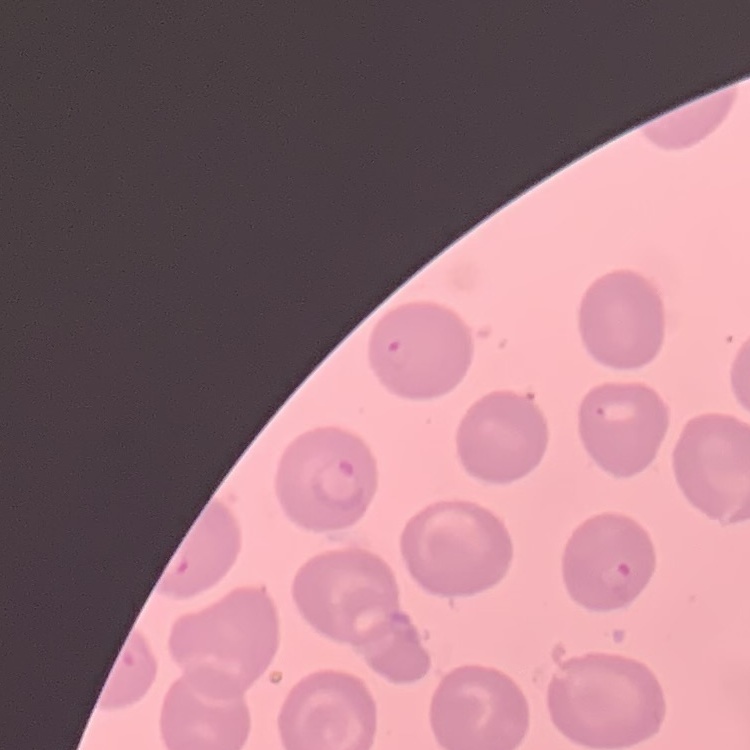
The erythrocytes show no rouleaux formation. One tile cut from a larger photomicrograph. Thin peripheral smear. Stained with either Field's or Giemsa.